Point out each malaria parasite.
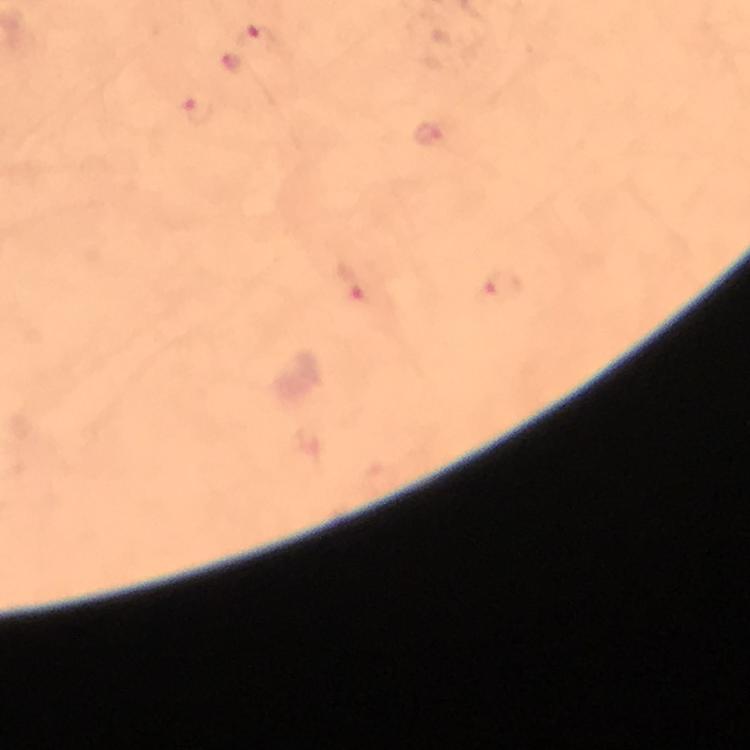

Approximate centers as (x, y) in pixels.
Malaria parasites: (258, 39), (200, 111), (426, 132), (358, 282), (503, 285).

capture = smartphone mounted on the microscope
image size = 750×750 pixels
cropped from = a single field of view
magnification = 100x
preparation = thick blood film
context = from a diagnostic examination for malaria
stain = Giemsa
immersion oil = used